Give the extent of all uninfected red blood cells.
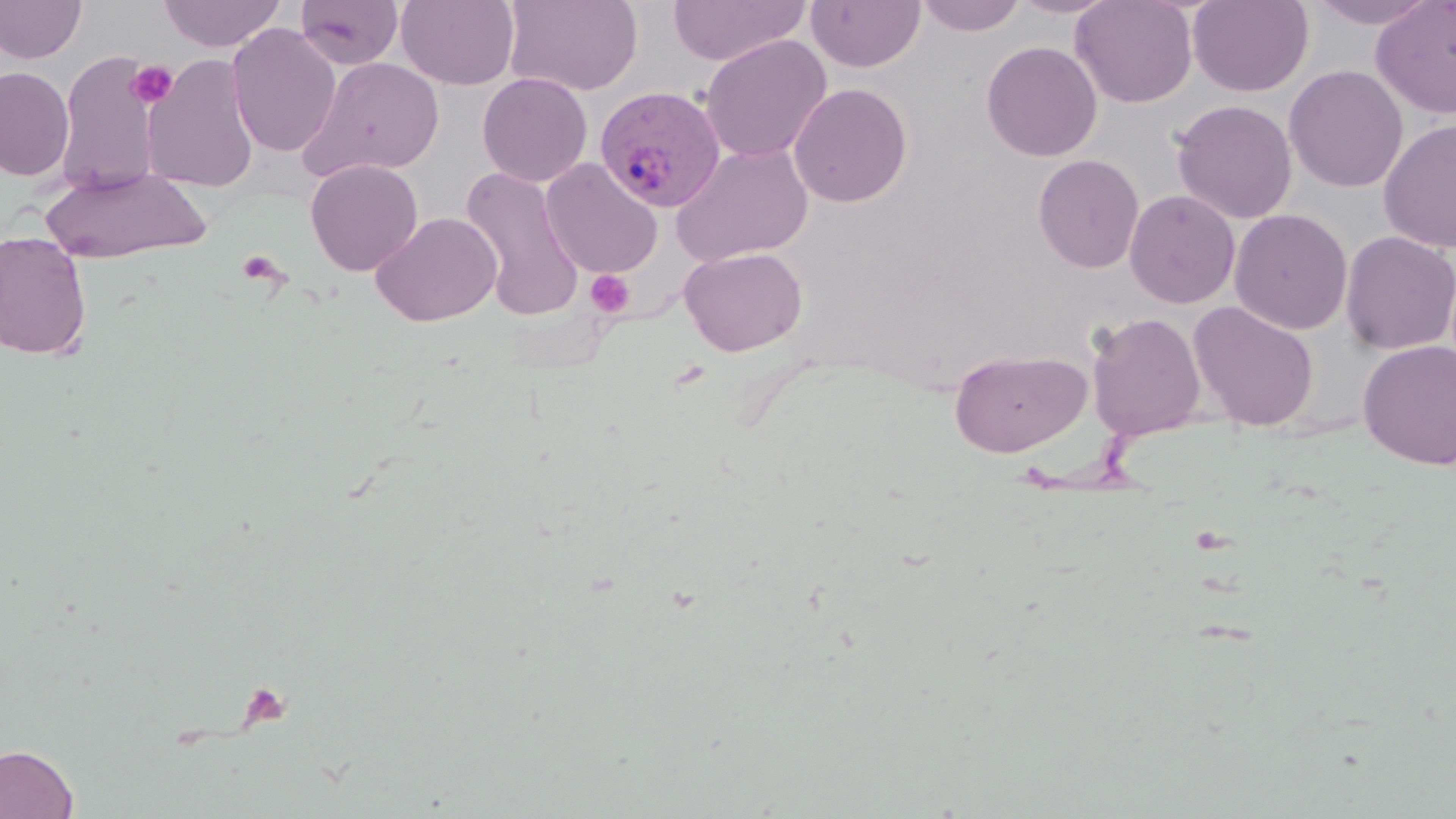

Approximate bounding boxes as (x1,y1)-(x2,y2) corner pairs in pixels.
Uninfected red blood cells: (0,0)-(87,64), (158,0)-(286,51), (294,0)-(404,70), (396,0)-(520,91), (504,0)-(643,96), (668,0)-(810,66), (805,0)-(925,73), (914,0)-(1028,36), (1009,0)-(1121,18), (1070,0)-(1198,108), (1187,0)-(1313,97), (1305,0)-(1443,29), (1370,1)-(1456,119), (226,23)-(341,157), (700,34)-(832,163), (981,41)-(1102,162), (55,51)-(163,196), (142,53)-(260,194), (300,57)-(445,181), (1284,65)-(1408,193), (0,67)-(74,181), (477,72)-(593,187), (789,82)-(913,207), (1171,99)-(1297,224), (1378,119)-(1456,253), (671,143)-(813,266), (1033,154)-(1144,274), (305,159)-(423,276), (541,159)-(663,279), (39,165)-(213,264), (459,165)-(584,319), (1124,190)-(1240,309), (1229,208)-(1352,335), (371,212)-(502,326), (0,231)-(93,359), (1340,231)-(1456,355), (680,246)-(807,356), (1188,301)-(1320,432), (1086,312)-(1205,440), (1358,340)-(1456,470), (949,350)-(1089,457), (0,743)-(79,819).

Platelet locations: (126,60)-(178,108), (235,248)-(289,291), (585,270)-(634,316). Plasmodium vivax-infected red blood cell locations: (594,86)-(726,213). Slide-level diagnosis: Plasmodium vivax. Single field of view. Optical microscopy. Thin blood film. 1000x magnification. May-Grünwald-Giemsa-stained preparation. Image is 1456×819 pixels.